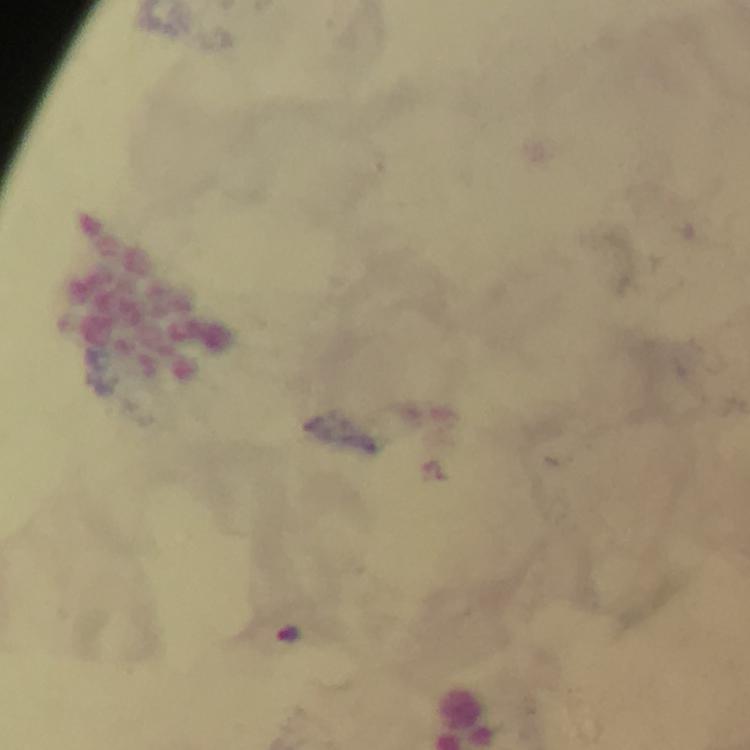

Approximate centers as [x, y] in pixels. Malaria parasite locations: [288, 635]. Thick blood film. Image is 750×750 pixels. From a malaria diagnostic workup. Cropped region of a single field of view. Giemsa stain. Photographed with a smartphone mounted on the microscope. Immersion oil was used. At 100x magnification.